Name the cell type shown.
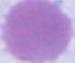

This is an erythrocyte.

modality = photomicrograph
magnification = 1000x